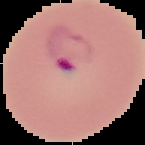 Cell region segmented out of the field of view; the surrounding area is masked to black. Image is 145×145 pixels. From a thin blood film. Malaria status: parasitized.